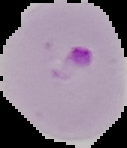
image_size: 127×148 pixels
image_type: segmented cell region on a black background
preparation: thin blood film
malaria_status: parasitized